Outline each blood parasite and name the species.
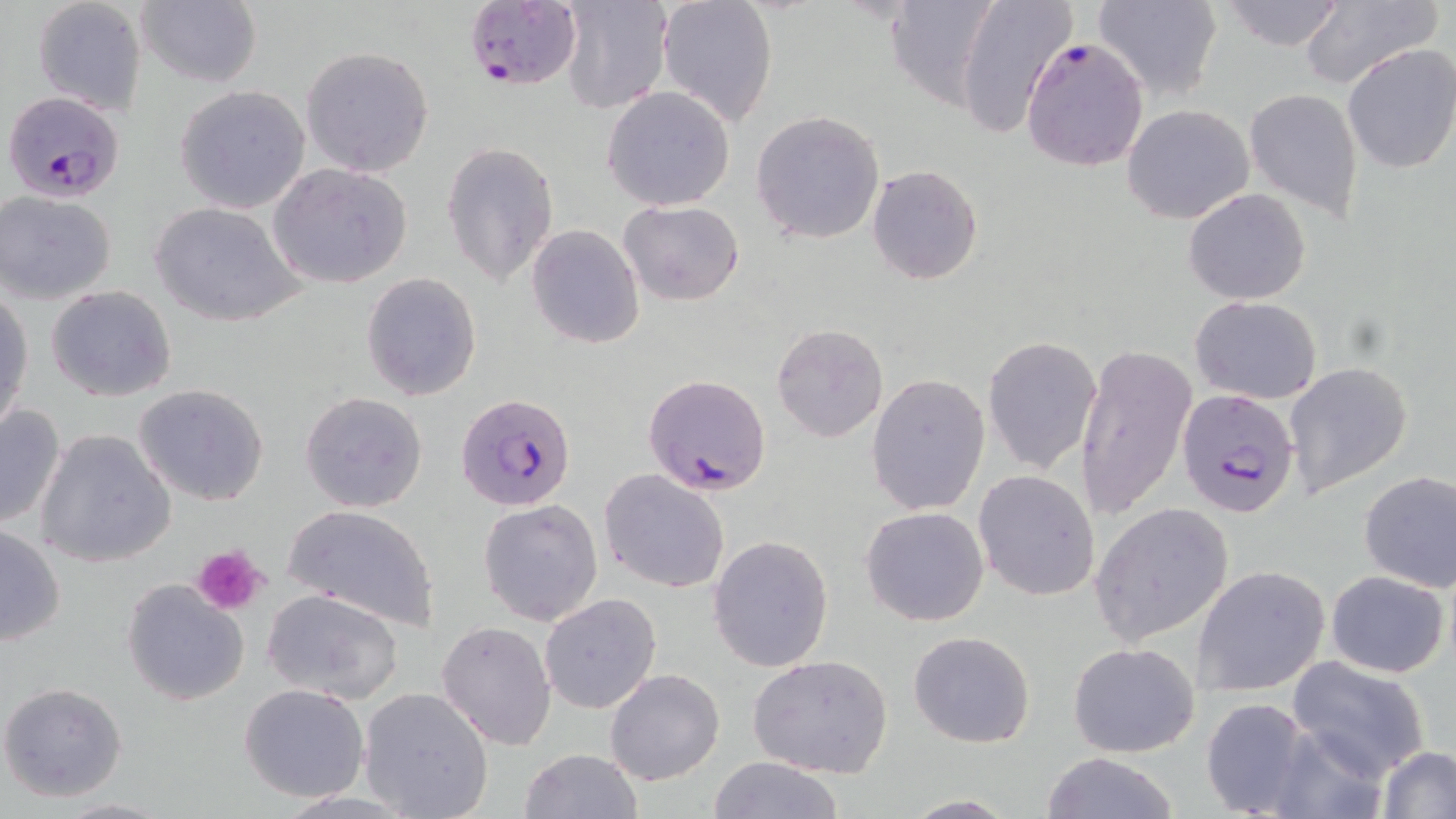
Approximate bounding boxes as (x1, y1, x2, y2) in pixels.
Plasmodium falciparum-infected red blood cells: (461, 0, 582, 93), (1020, 37, 1149, 172), (3, 89, 125, 200), (644, 374, 772, 496), (1177, 388, 1301, 519), (457, 392, 577, 513).
No Plasmodium ovale, Plasmodium malariae, Plasmodium vivax, Babesia divergens, or Trypanosoma brucei observed.

Summary:
  - Platelet locations: (191, 544, 268, 617)
  - Uninfected red blood cell locations: (656, 0, 780, 128), (953, 0, 1078, 139), (1091, 0, 1223, 102), (1217, 0, 1349, 52), (31, 1, 147, 115), (135, 1, 262, 88), (559, 2, 673, 116), (1297, 2, 1442, 89), (884, 4, 998, 109), (1340, 43, 1456, 175), (300, 45, 435, 178), (173, 84, 314, 213), (602, 86, 736, 210), (1244, 88, 1363, 221), (1122, 104, 1256, 224), (751, 110, 885, 245), (442, 142, 560, 289), (268, 163, 413, 289), (867, 166, 982, 284), (1182, 188, 1312, 306), (1, 192, 118, 303), (149, 200, 306, 327), (619, 200, 745, 306), (527, 224, 645, 350), (360, 272, 482, 400), (46, 286, 178, 402), (1, 290, 34, 433), (1190, 296, 1322, 403), (772, 324, 888, 442), (983, 336, 1102, 473), (1075, 344, 1199, 521), (1283, 360, 1414, 499), (867, 374, 990, 515), (133, 383, 270, 506), (299, 391, 429, 514), (0, 401, 67, 531), (35, 429, 177, 568), (599, 468, 731, 593), (1357, 468, 1456, 596), (974, 470, 1100, 601), (478, 499, 604, 627), (1090, 502, 1234, 648), (280, 504, 441, 632), (861, 506, 988, 627), (0, 524, 66, 645), (708, 535, 834, 672), (1193, 564, 1331, 695), (1326, 569, 1450, 677), (122, 578, 250, 707), (261, 589, 408, 707), (540, 594, 661, 713), (435, 620, 557, 750), (908, 630, 1036, 749), (1067, 641, 1201, 758), (747, 654, 895, 778), (1284, 658, 1433, 781), (605, 668, 725, 786), (0, 682, 128, 802), (239, 683, 369, 803), (358, 686, 493, 819), (1200, 697, 1322, 819), (1376, 746, 1456, 818), (518, 749, 642, 819), (1040, 752, 1181, 819), (707, 757, 847, 818), (897, 795, 1022, 817), (55, 797, 170, 818)
  - Slide-level diagnosis: Plasmodium falciparum
  - Preparation: thin blood smear
  - Stain: May-Grünwald-Giemsa
  - Image size: 1456×819 pixels
  - Field of view: single
  - Magnification: 1000x
  - Modality: light microscopy